Classify this cell by malaria status.
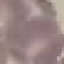

Uninfected.

Automatically extracted cell patch, resized to 64 × 64 pixels. Thin smear of blood. Giemsa stain. Photographed with a smartphone camera at the microscope eyepiece.